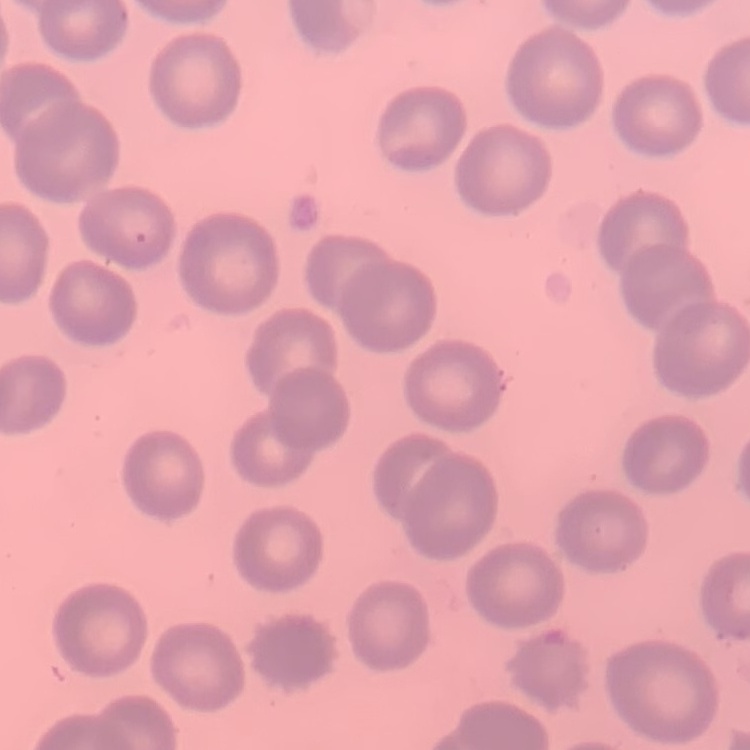 The red blood cells exhibit no rouleaux formation. One tile cut from a larger photomicrograph. Thin blood smear. Field's or Giemsa stain.